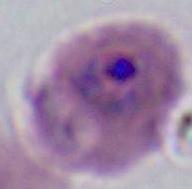

modality = photomicrograph
identification = Plasmodium
magnification = 400x or 1000x